Assess this cell for malaria.
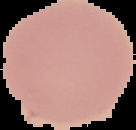

Uninfected.

From a thin blood film. Image is 136×130 pixels. Cell region segmented out of the field of view; the surrounding area is masked to black.